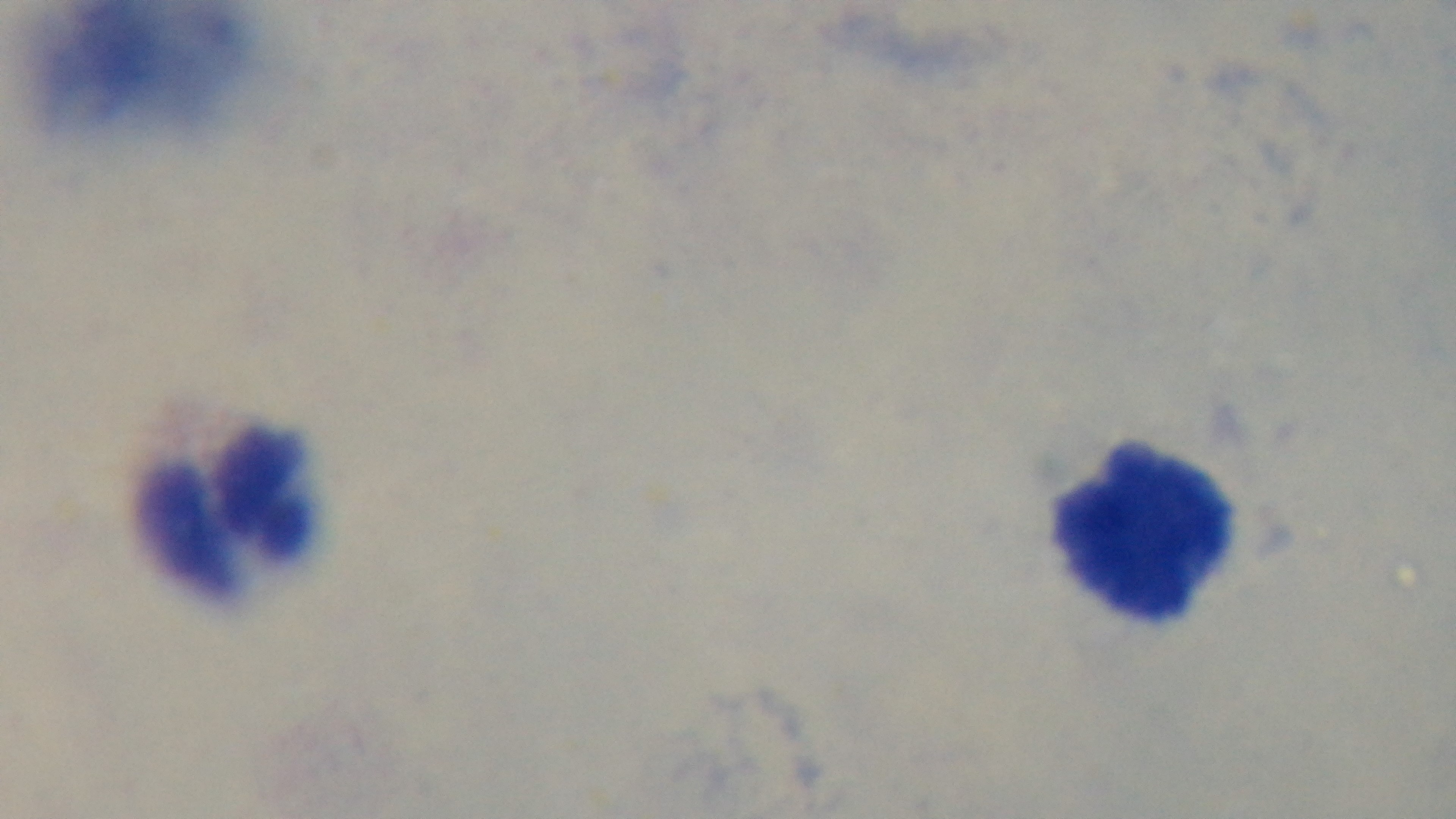
Summary:
  - Preparation: thick blood film
  - Malaria status: negative
  - Modality: light microscopy
  - Objective: 100x oil immersion
  - Capture: mounted 4K digital camera
  - Stain: Giemsa
  - Field of view: single